Look for Plasmodium parasites.
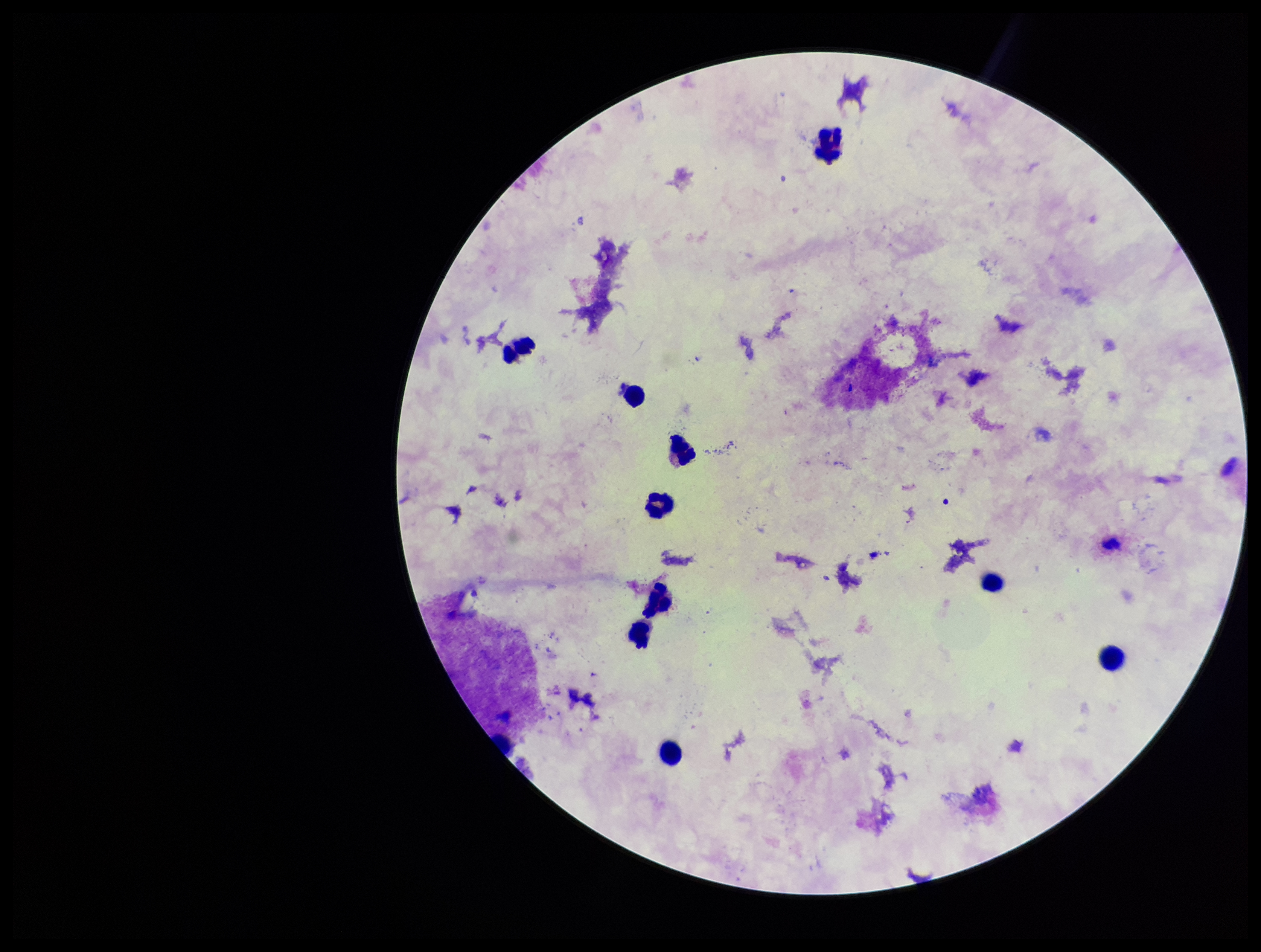
None detected.

Giemsa stain. Patient malaria status: negative. Preparation: thick. Image is 1261×952 pixels. Parasite count: 0. One field from this slide. Photographed through the microscope eyepiece with a smartphone camera. Leukocyte count: 10.